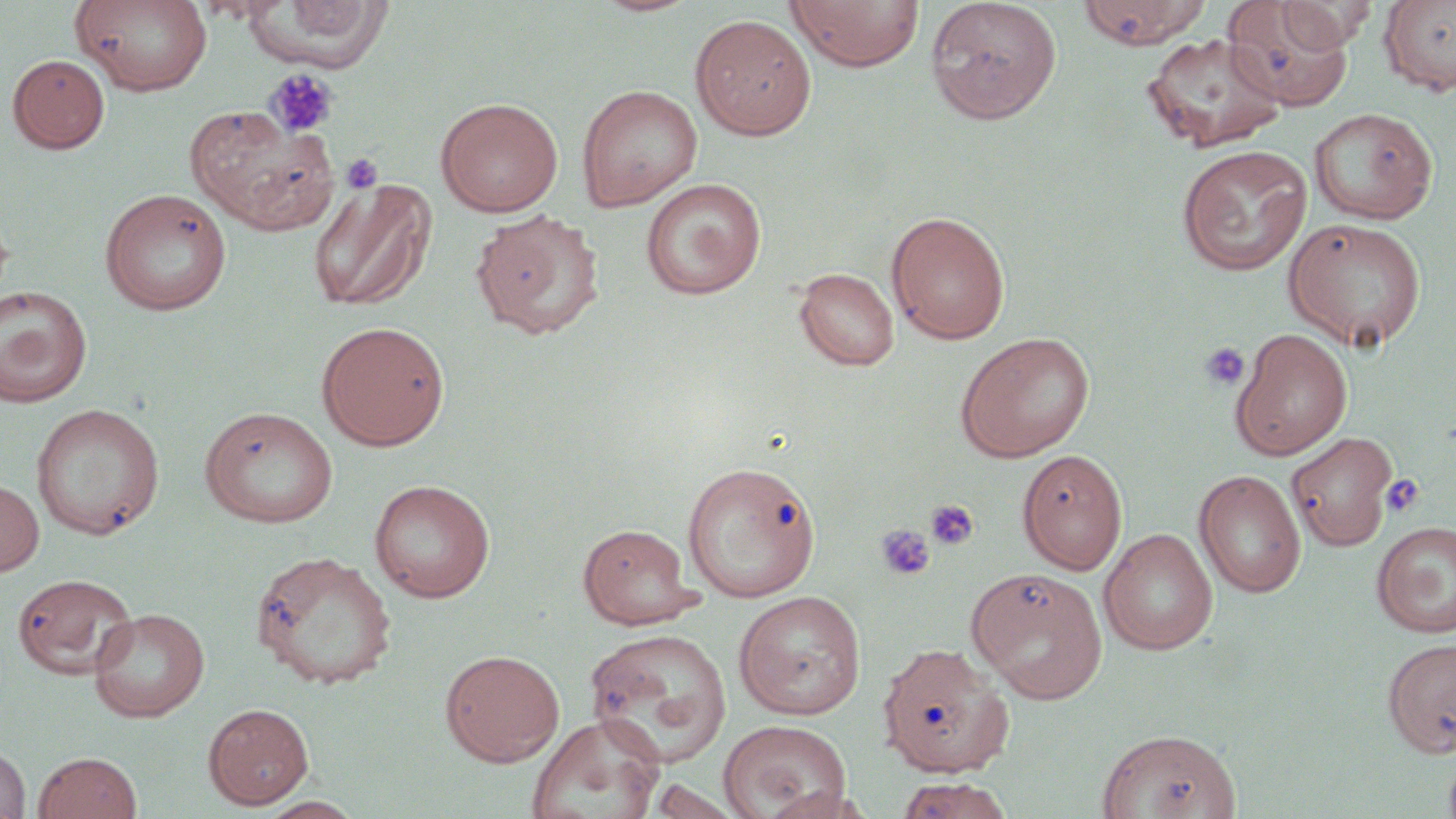
Summary:
  - Coordinate format: approximate bounding boxes as (x1, y1, x2, y2) in pixels
  - Uninfected red blood cell locations: (245, 0, 395, 70), (589, 0, 702, 17), (786, 0, 925, 73), (925, 0, 1062, 125), (1076, 0, 1211, 49), (1379, 0, 1456, 96), (72, 1, 212, 96), (1222, 1, 1352, 111), (1275, 1, 1376, 51), (690, 13, 817, 140), (1140, 32, 1287, 152), (7, 54, 110, 153), (576, 84, 703, 212), (435, 97, 564, 217), (185, 105, 339, 234), (1308, 107, 1438, 225), (1175, 144, 1313, 276), (641, 177, 767, 300), (307, 178, 437, 314), (99, 187, 232, 315), (470, 208, 605, 340), (886, 211, 1010, 345), (1283, 216, 1428, 352), (794, 267, 899, 371), (0, 286, 93, 407), (316, 320, 450, 451), (1230, 327, 1353, 461), (955, 331, 1095, 462), (30, 402, 165, 540), (199, 405, 338, 528), (1286, 431, 1398, 552), (1017, 449, 1128, 575), (681, 459, 821, 602), (1193, 470, 1306, 598), (369, 478, 496, 602), (0, 479, 44, 577), (1372, 521, 1456, 638), (577, 523, 702, 630), (1098, 528, 1218, 655), (249, 550, 398, 688), (967, 568, 1108, 704), (13, 572, 137, 679), (733, 590, 867, 720), (88, 607, 210, 722), (584, 628, 733, 768), (1382, 637, 1456, 759), (882, 646, 1020, 782), (440, 649, 565, 765), (203, 702, 314, 809), (526, 713, 666, 819), (718, 719, 852, 819), (1095, 727, 1242, 818), (0, 744, 31, 819), (1442, 749, 1456, 819), (33, 751, 143, 819), (895, 776, 1015, 819), (647, 778, 746, 819), (255, 796, 367, 819)
  - Platelet locations: (264, 68, 339, 139), (340, 153, 385, 194), (1199, 342, 1250, 390), (1380, 474, 1425, 518), (924, 498, 980, 551), (875, 524, 936, 582)
  - Slide-level diagnosis: no evidence of blood parasites
  - Image size: 1456×819 pixels
  - Magnification: 1000x
  - Modality: optical microscopy
  - Field of view: one of a larger specimen
  - Preparation: thin blood smear
  - Stain: May-Grünwald-Giemsa